Report the malaria status of this cell.
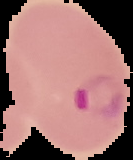
It is parasitized.

{
  "image_size": "133×160 pixels",
  "image_type": "segmented cell region on a black background",
  "preparation": "thin blood film"
}